Find the cells and give the type of each one.
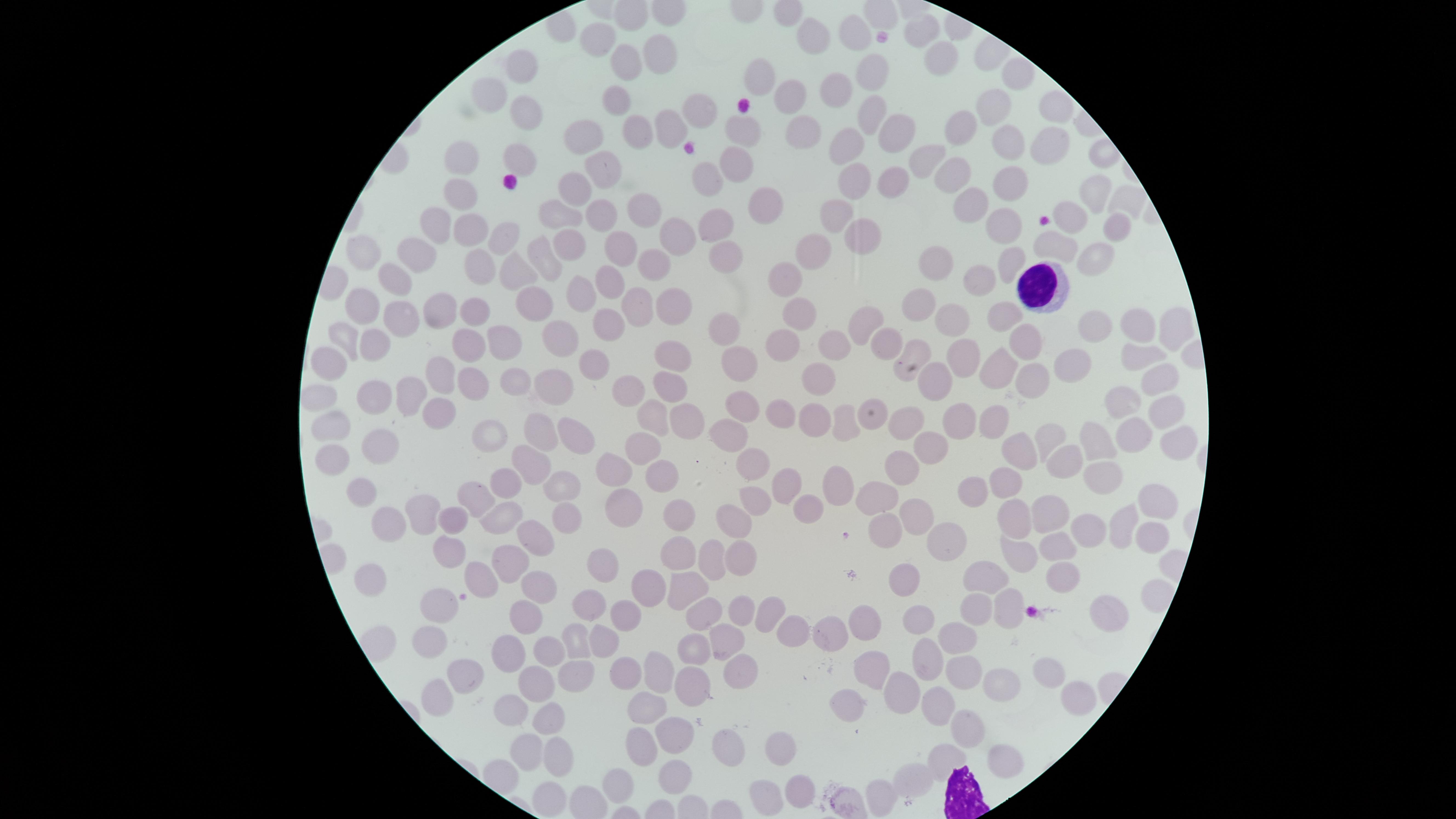

No parasitized red blood cells identified.
Approximate marker points as (x, y) in pixels.
Uninfected red blood cells: (922, 28), (854, 35), (808, 36), (594, 37), (657, 52), (944, 59), (625, 63), (518, 65), (873, 71), (1017, 71), (759, 78), (827, 85), (787, 93), (614, 95), (482, 98), (696, 106), (986, 107), (1050, 108), (870, 112), (525, 116), (956, 127), (668, 130), (799, 131), (888, 132), (738, 133), (637, 137), (584, 138), (1005, 145), (1048, 145), (847, 146), (521, 155), (927, 156), (738, 159), (462, 162), (601, 169), (709, 176), (956, 176), (862, 182), (894, 186), (1007, 186), (575, 188), (1092, 191), (461, 196), (1123, 200), (758, 202), (967, 205), (641, 208), (559, 209), (598, 212), (839, 213), (1000, 216), (1070, 218), (437, 222), (714, 222), (466, 228), (1111, 229), (674, 237), (860, 237), (503, 239), (575, 242), (1046, 245), (622, 249), (818, 250), (543, 252), (416, 253), (365, 255), (1089, 258), (1008, 259), (650, 261), (722, 261), (938, 262), (478, 265), (517, 270), (782, 274), (393, 276), (607, 279), (980, 281), (581, 291), (666, 301), (642, 302), (350, 304), (917, 305), (436, 307), (532, 307), (474, 311), (804, 314), (996, 314), (391, 319), (1135, 319), (866, 320), (600, 321), (947, 324), (1092, 329), (729, 330), (1167, 330), (342, 334), (504, 337), (556, 337), (785, 340), (373, 341), (462, 342), (831, 342), (881, 342), (1019, 343), (914, 354), (670, 355), (962, 357), (1136, 358), (332, 360), (1068, 362), (742, 365), (587, 368), (996, 368), (437, 371), (817, 380), (1026, 380), (1157, 381), (939, 383), (475, 385), (513, 387), (623, 388), (552, 389), (668, 389), (410, 390), (376, 392), (315, 397), (1124, 401), (740, 404), (1164, 411), (782, 412), (649, 416), (438, 417), (872, 417), (687, 421), (812, 421), (847, 421), (904, 421), (993, 421), (957, 423), (335, 427), (491, 433), (540, 433), (734, 433), (568, 435), (1133, 435), (1050, 436), (1094, 437), (1170, 439), (924, 444), (386, 447), (1021, 450), (639, 453), (330, 458), (1066, 460), (525, 464), (900, 465), (748, 470), (614, 471), (661, 474), (1101, 477), (505, 485), (556, 485), (1006, 485), (783, 487), (839, 487), (361, 490), (878, 493), (970, 494), (477, 499), (746, 500), (1153, 502), (622, 505), (1051, 506), (806, 508), (415, 515), (676, 516), (917, 516), (568, 518), (454, 520), (1016, 520), (732, 522), (494, 523), (382, 525), (1122, 528), (1085, 531), (885, 532), (948, 539), (1146, 539), (531, 542), (1056, 546), (1013, 550), (448, 552), (678, 554), (714, 560), (742, 561), (504, 563), (600, 565), (480, 575), (372, 577), (905, 577), (991, 577), (532, 580), (1069, 580), (646, 584), (686, 590), (1148, 597), (435, 600), (587, 603), (1004, 605), (975, 607), (739, 609), (763, 612), (521, 613), (1110, 614), (627, 615), (707, 615), (918, 618), (864, 622), (795, 629), (833, 633), (577, 638), (958, 638), (428, 641), (603, 641), (726, 644), (549, 646), (692, 650), (508, 657), (933, 663), (659, 666), (961, 668), (736, 669), (873, 669), (627, 670), (1047, 671), (574, 673), (463, 675), (694, 681), (534, 684), (999, 688), (903, 689), (436, 698), (1078, 699), (646, 707), (512, 708), (938, 708), (851, 709), (549, 717), (970, 728), (674, 734), (638, 743), (781, 747), (729, 751), (523, 752), (1009, 759), (554, 760), (941, 760), (676, 776), (915, 777), (617, 785), (798, 794), (883, 795), (552, 798), (767, 799).
White blood cells: (1032, 283).

preparation = thin blood smear
stain = Giemsa
visible region = circular
image size = 1456×819 pixels
field of view = single
capture = smartphone photograph through the microscope eyepiece